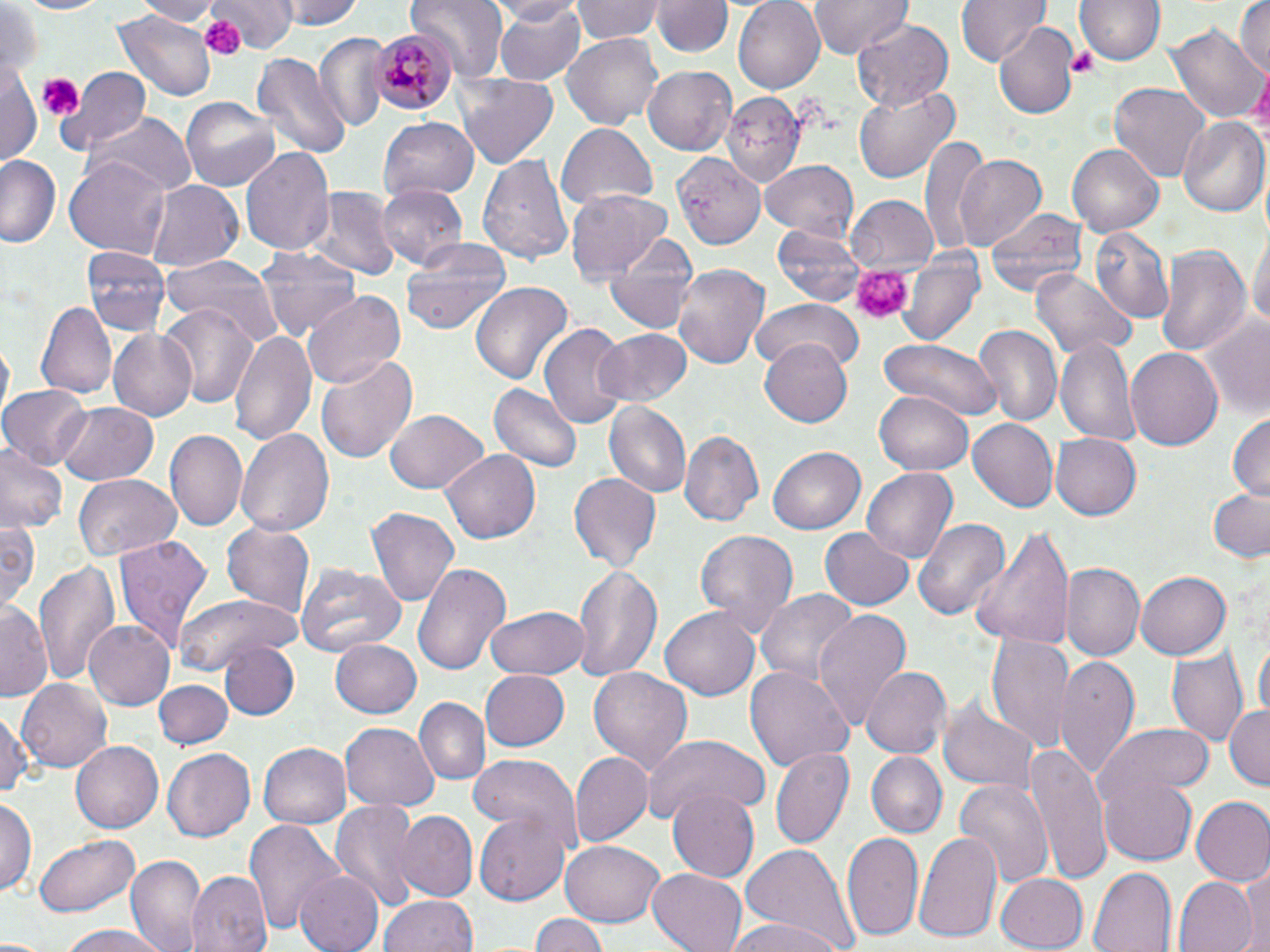

Approximate bounding boxes as (x1, y1, x2, y2) in pixels. Platelet locations: (200, 13, 246, 60), (1068, 47, 1101, 79), (35, 74, 82, 124), (850, 265, 912, 326). Uninfected red blood cell locations: (11, 0, 111, 16), (136, 0, 222, 26), (211, 0, 291, 50), (279, 0, 361, 30), (411, 0, 506, 78), (483, 0, 582, 25), (489, 0, 588, 85), (572, 0, 665, 43), (733, 0, 826, 93), (808, 0, 910, 59), (958, 0, 1049, 69), (1077, 0, 1163, 67), (1234, 0, 1270, 80), (654, 1, 731, 60), (2, 3, 42, 82), (113, 11, 215, 102), (852, 20, 954, 109), (995, 23, 1078, 119), (1170, 24, 1265, 124), (314, 32, 389, 132), (562, 34, 664, 129), (252, 51, 351, 158), (0, 58, 40, 167), (642, 66, 737, 155), (57, 67, 151, 155), (455, 73, 559, 172), (1109, 82, 1212, 180), (853, 84, 961, 182), (722, 91, 806, 184), (181, 93, 280, 188), (89, 112, 196, 193), (1179, 115, 1269, 215), (378, 116, 481, 202), (557, 125, 658, 211), (921, 137, 995, 256), (1068, 144, 1163, 235), (241, 146, 334, 256), (670, 149, 767, 252), (477, 153, 574, 266), (953, 153, 1047, 248), (0, 155, 59, 249), (66, 155, 169, 255), (760, 161, 861, 239), (147, 181, 243, 271), (378, 184, 468, 272), (312, 186, 401, 282), (566, 189, 674, 281), (847, 196, 937, 274), (986, 204, 1087, 303), (1250, 222, 1269, 338), (771, 224, 866, 307), (1090, 226, 1174, 326), (605, 230, 699, 335), (403, 237, 512, 335), (1152, 243, 1250, 358), (82, 246, 170, 337), (257, 246, 360, 346), (161, 253, 282, 344), (899, 253, 985, 347), (672, 262, 770, 372), (1030, 267, 1135, 361), (469, 282, 574, 388), (302, 289, 407, 390), (752, 299, 865, 371), (38, 300, 116, 399), (160, 301, 259, 409), (1198, 313, 1270, 418), (540, 321, 629, 433), (971, 324, 1063, 427), (596, 327, 694, 407), (107, 328, 197, 421), (230, 328, 314, 446), (1056, 336, 1140, 448), (880, 337, 1002, 419), (2, 339, 15, 416), (760, 343, 852, 427), (1125, 346, 1224, 451), (316, 354, 419, 466), (1, 384, 90, 470), (489, 384, 582, 473), (875, 390, 973, 474), (604, 402, 690, 499), (58, 403, 159, 484), (385, 409, 487, 496), (1227, 412, 1270, 502), (966, 417, 1058, 512), (235, 427, 338, 537), (680, 428, 763, 527), (165, 431, 248, 533), (1052, 433, 1142, 519), (768, 444, 866, 532), (0, 445, 65, 535), (442, 448, 543, 544), (865, 467, 958, 563), (568, 474, 660, 570), (72, 475, 181, 562), (1208, 489, 1270, 566), (364, 507, 460, 608), (913, 515, 1009, 625), (0, 518, 39, 616), (220, 522, 315, 618), (969, 525, 1074, 653), (820, 527, 912, 610), (695, 529, 796, 631), (113, 534, 214, 652), (33, 560, 117, 687), (296, 561, 407, 656), (413, 563, 512, 675), (1062, 563, 1144, 662), (570, 565, 662, 683), (1135, 571, 1230, 660), (759, 589, 859, 687), (173, 593, 300, 671), (0, 602, 54, 698), (484, 606, 588, 679), (660, 606, 759, 700), (813, 609, 914, 729), (85, 619, 176, 711), (988, 631, 1074, 752), (330, 639, 421, 717), (1254, 639, 1269, 725), (220, 640, 300, 720), (1169, 646, 1246, 747), (1054, 656, 1138, 776), (743, 664, 854, 769), (861, 666, 950, 757), (586, 668, 694, 777), (477, 669, 569, 752), (16, 677, 112, 773), (155, 679, 231, 751), (939, 692, 1039, 795), (414, 696, 491, 786), (1223, 701, 1270, 789), (0, 707, 31, 807), (1101, 722, 1215, 799), (340, 723, 439, 811), (639, 733, 770, 824), (260, 740, 353, 827), (71, 741, 162, 832), (1026, 743, 1112, 885), (771, 746, 853, 848), (162, 748, 255, 842), (868, 751, 946, 837), (569, 752, 653, 848), (467, 753, 582, 848), (1099, 771, 1198, 865), (954, 780, 1052, 888), (669, 786, 762, 881), (1191, 796, 1270, 885), (0, 797, 35, 897), (328, 799, 422, 912), (391, 810, 478, 902), (476, 812, 573, 906), (244, 819, 344, 934), (914, 829, 1004, 945), (841, 831, 924, 944), (35, 834, 140, 917), (560, 838, 664, 926), (740, 844, 856, 952), (127, 853, 208, 952), (1088, 865, 1177, 952), (647, 866, 751, 952), (1237, 866, 1269, 950), (294, 869, 385, 952), (186, 871, 273, 952), (995, 872, 1089, 950), (1174, 877, 1257, 952), (380, 895, 477, 952), (530, 912, 605, 952), (721, 918, 849, 952), (59, 925, 171, 952). Plasmodium malariae-infected red blood cell locations: (371, 27, 455, 113). Slide-level diagnosis: Plasmodium malariae. Light microscopy. Thin blood smear. One field of a larger specimen. Image is 1270×952 pixels. May-Grünwald-Giemsa-stained preparation. Captured at 1000x magnification.